Classify this cell by malaria status.
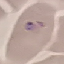

It is parasitized.

stain = Giemsa
capture = smartphone camera at the microscope eyepiece
image type = automatically extracted cell patch, resized to 64 × 64 pixels
preparation = thin blood smear